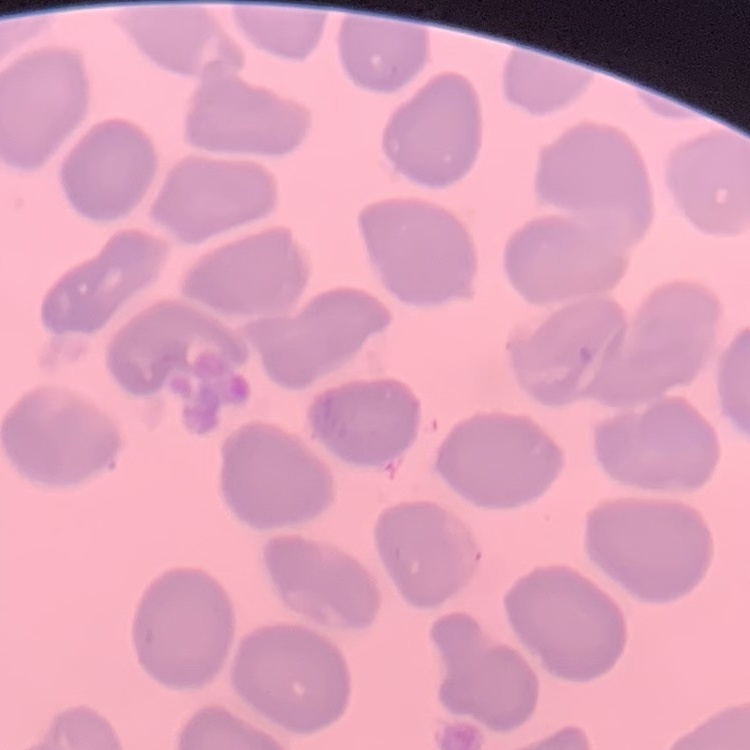
The red blood cells show no rouleaux formation. Square crop of a larger photomicrograph. Stained with either Field's or Giemsa. Thin blood smear.